Assess this cell for malaria.
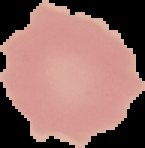
Uninfected.

preparation = thin blood film
image size = 145×148 pixels
image type = cell region segmented out of the field of view; surrounding area masked to black